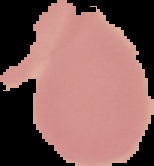 From a thin blood smear. Image is 154×166 pixels. The area outside the segmented cell region is set to black. Result: no Plasmodium parasites detected.